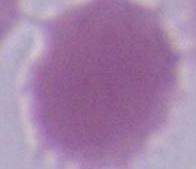

1000x magnification. An erythrocyte is seen. Micrograph.